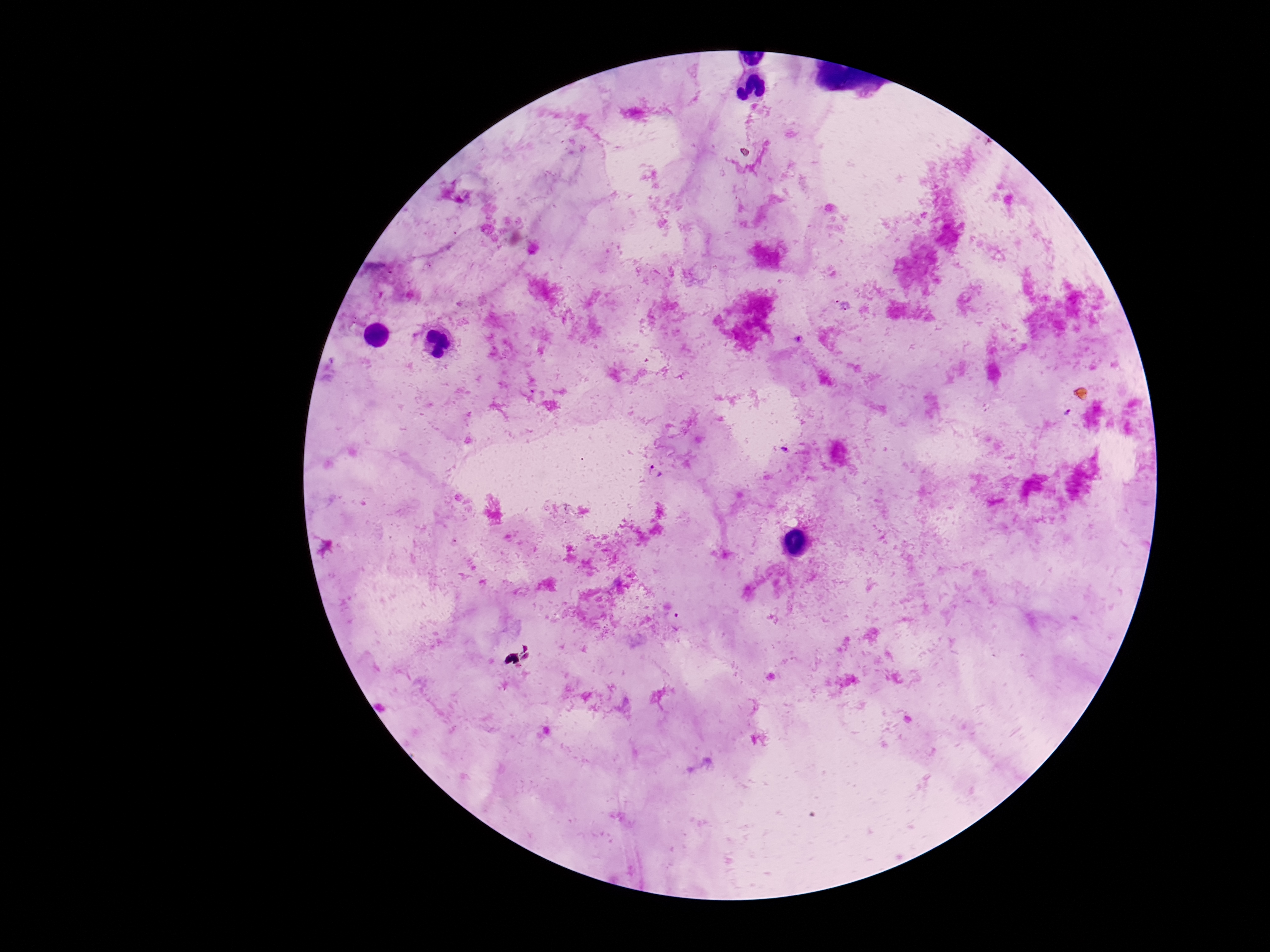 Approximate centers as [x, y] in pixels. Plasmodium parasite locations: [1069, 412], [655, 472]. Smartphone photograph taken through the microscope eyepiece. Thick blood film. 100x magnification. Giemsa stain. One field from this slide. Patient malaria status: infected. Image is 1270×952 pixels.